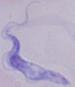 A trypanosome is seen. 1000x magnification. Micrograph.